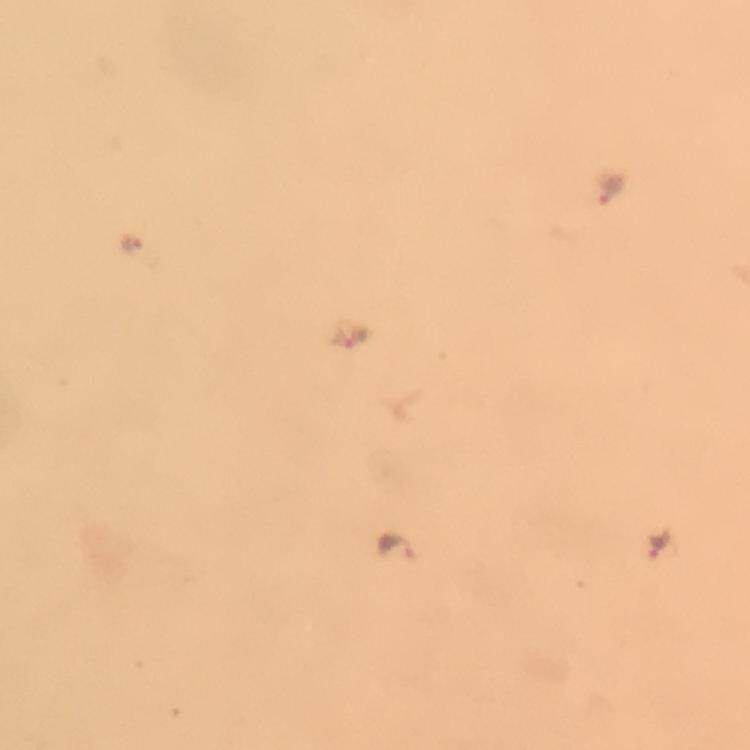

Approximate object centers, in pixels from the top-left corner.
Summary:
  - Malaria parasite locations: (x=609, y=187), (x=137, y=245), (x=351, y=337), (x=655, y=543), (x=393, y=547)
  - Image size: 750×750 pixels
  - Context: from a malaria diagnostic workup
  - Immersion oil: used
  - Cropped from: a single field of view
  - Magnification: 100x
  - Capture: smartphone camera through the microscope
  - Stain: Giemsa
  - Preparation: thick blood film